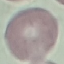
result: negative for malaria parasites
preparation: thin blood film
capture: smartphone camera at the microscope eyepiece
image_type: cell patch, automatically extracted from a larger field of view and resized to 64 × 64 pixels
stain: Giemsa